Report the malaria status of this cell.
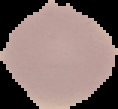
Uninfected.

Summary:
  - Image size: 118×109 pixels
  - Image type: segmented cell region with the area outside set to black
  - Preparation: thin blood film